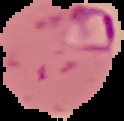

Summary:
  - Preparation: thin blood film
  - Image type: segmented cell region with the area outside set to black
  - Malaria status: parasitized
  - Image size: 124×121 pixels